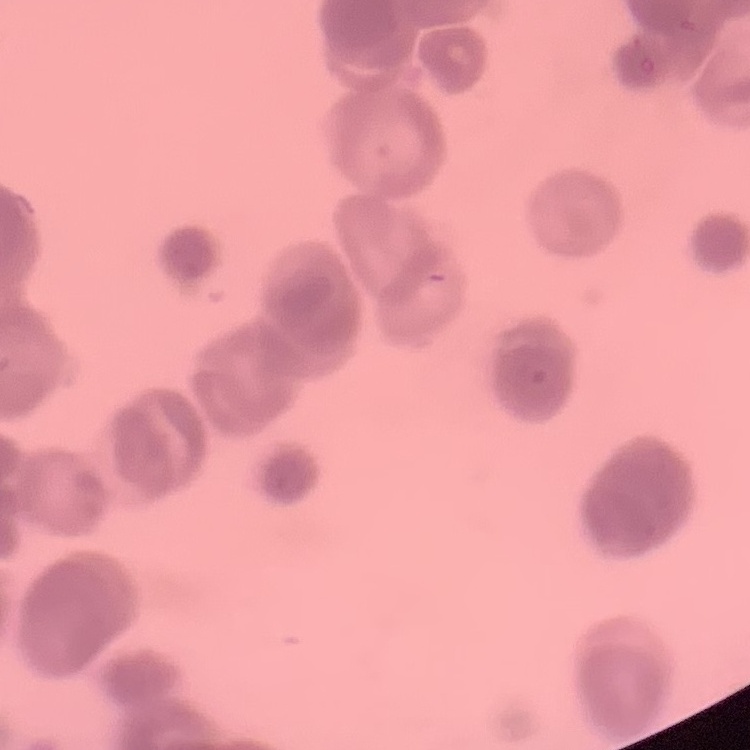

red_blood_cell_morphology: rouleaux formation
stain: Field's or Giemsa
preparation: thin peripheral smear
image_type: square crop of a larger photomicrograph